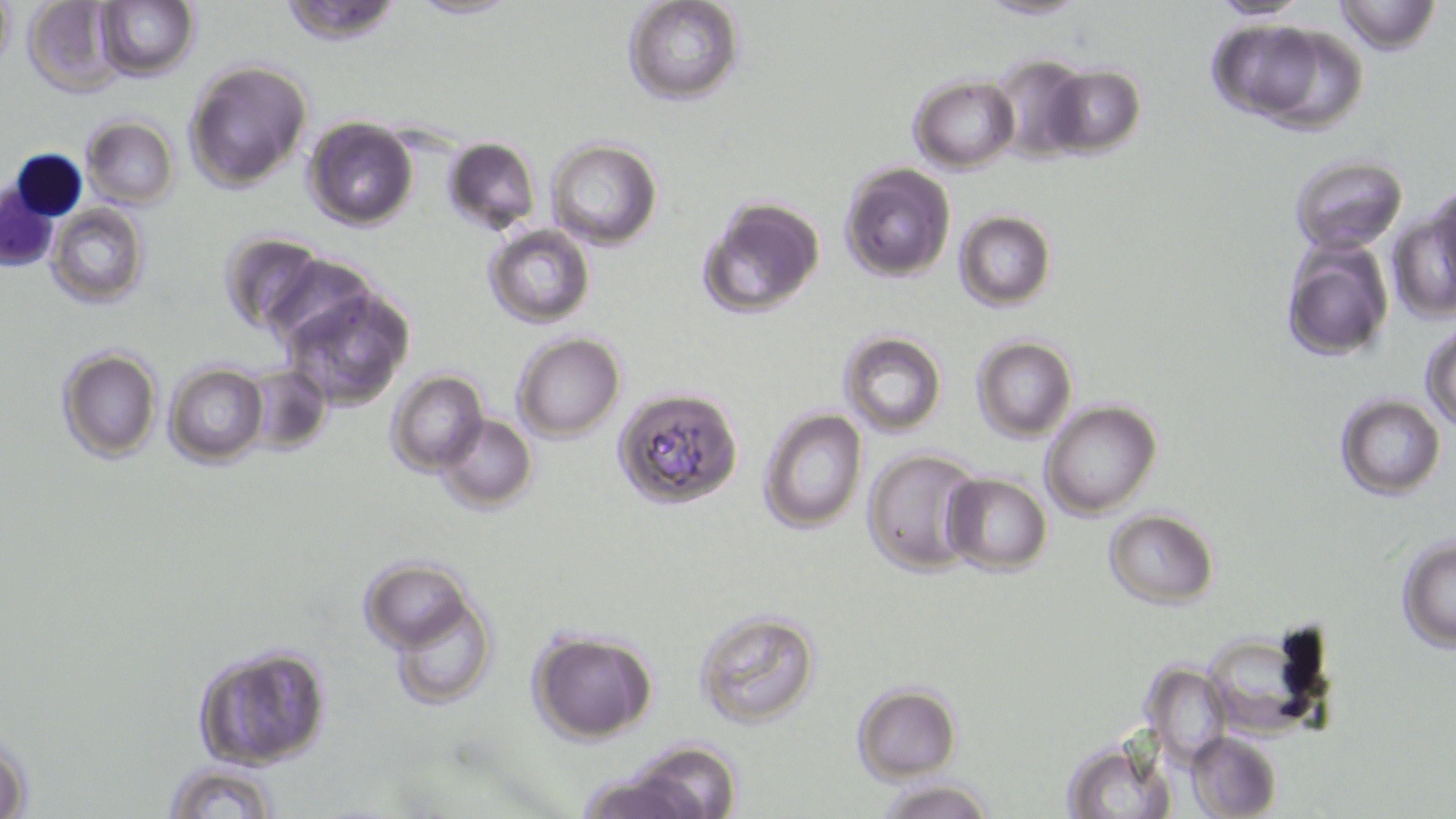

Approximate bounding boxes as [x1, y1, x2, y2] in pixels. Uninfected red blood cell locations: [0, 0, 15, 69], [22, 0, 127, 96], [276, 0, 405, 43], [407, 0, 521, 20], [974, 0, 1093, 20], [1205, 0, 1316, 21], [1334, 0, 1440, 54], [95, 1, 199, 80], [622, 1, 745, 105], [1206, 20, 1366, 137], [988, 54, 1094, 164], [183, 61, 311, 189], [1043, 66, 1146, 158], [910, 76, 1019, 172], [82, 117, 179, 208], [302, 118, 418, 230], [442, 138, 541, 236], [546, 138, 663, 250], [1287, 155, 1409, 257], [840, 165, 955, 281], [1428, 183, 1456, 303], [696, 195, 825, 321], [1394, 196, 1456, 318], [48, 205, 149, 308], [955, 212, 1055, 310], [484, 224, 594, 328], [217, 231, 326, 339], [1282, 237, 1393, 364], [264, 253, 380, 352], [283, 286, 414, 410], [1422, 325, 1456, 431], [513, 332, 626, 442], [839, 333, 947, 438], [973, 336, 1077, 441], [57, 348, 162, 464], [164, 363, 267, 466], [246, 364, 333, 455], [387, 371, 488, 476], [614, 386, 745, 510], [1335, 394, 1446, 499], [1041, 400, 1162, 519], [757, 408, 867, 533], [437, 413, 535, 511], [863, 448, 984, 575], [942, 473, 1052, 575], [1103, 509, 1219, 607], [1397, 537, 1456, 650], [363, 558, 473, 651], [388, 593, 498, 710], [693, 608, 822, 731], [1199, 624, 1336, 742], [527, 629, 658, 743], [192, 642, 332, 769], [1143, 664, 1232, 767], [851, 685, 960, 781], [0, 726, 34, 819], [1186, 731, 1281, 819], [618, 740, 744, 817], [1060, 740, 1177, 818], [161, 760, 282, 819], [574, 772, 703, 819], [875, 777, 995, 819]. White blood cell locations: [1, 147, 86, 271]. Slide-level diagnosis: Plasmodium falciparum. One field of a larger specimen. Image is 1456×819 pixels. 1000x magnification. Thin blood film. May-Grünwald-Giemsa stain. Optical microscopy.